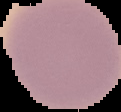

Summary:
  - Result: no Plasmodium parasites detected
  - Preparation: thin blood film
  - Image type: cell region segmented out of the field of view; surrounding area masked to black
  - Image size: 121×112 pixels